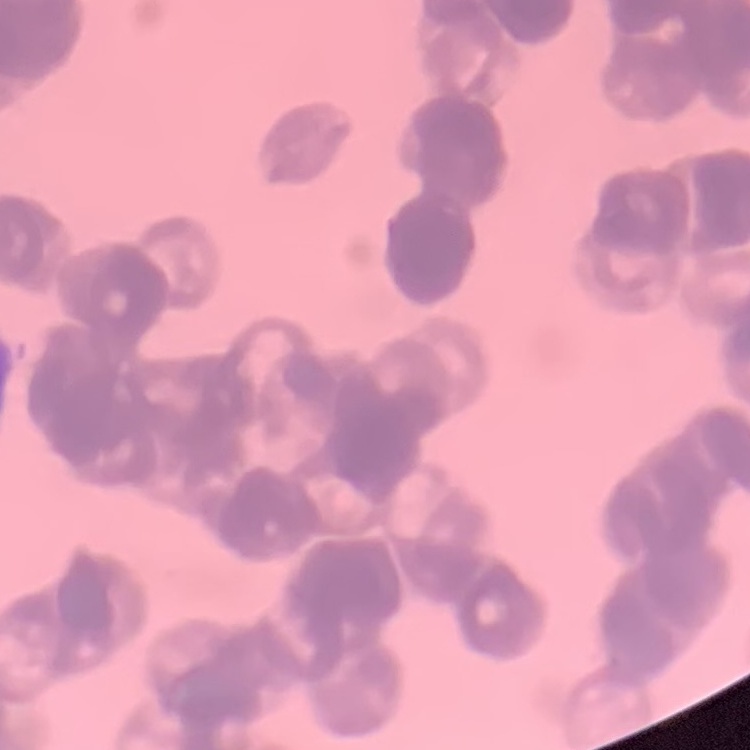

The erythrocytes show rouleaux formation. Square crop of a larger photomicrograph. Thin blood smear. Stained with either Field's or Giemsa.